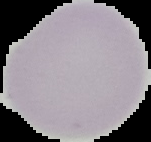 Image is 151×142 pixels. Malaria status: uninfected. Cell region segmented out of the field of view; the surrounding area is masked to black. From a thin blood film.